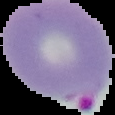
Summary:
  - Image size: 115×115 pixels
  - Malaria status: parasitized
  - Image type: segmented cell region on a black background
  - Preparation: thin blood smear